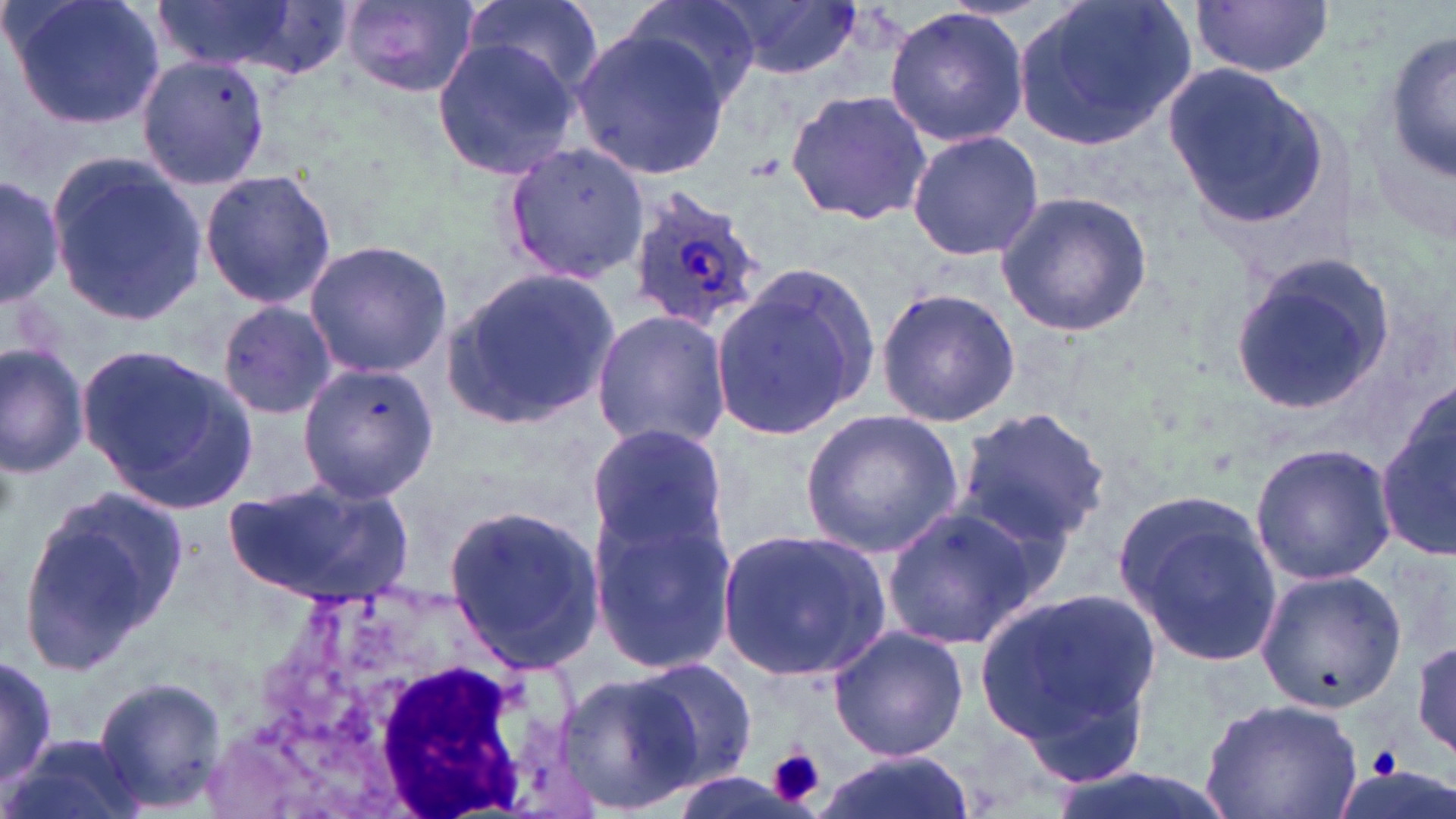
Summary:
  - Coordinate format: approximate bounding boxes as named x1/y1/x2/y2 corners in pixels
  - White blood cell locations: (x1=214, y1=587, x2=596, y2=819)
  - Plasmodium ovale-infected red blood cell locations: (x1=624, y1=186, x2=766, y2=335)
  - Uninfected red blood cell locations: (x1=6, y1=0, x2=165, y2=132), (x1=152, y1=0, x2=304, y2=74), (x1=336, y1=0, x2=482, y2=96), (x1=463, y1=0, x2=603, y2=97), (x1=624, y1=0, x2=761, y2=108), (x1=717, y1=0, x2=862, y2=81), (x1=1015, y1=0, x2=1194, y2=149), (x1=1191, y1=0, x2=1335, y2=78), (x1=883, y1=7, x2=1030, y2=145), (x1=571, y1=28, x2=733, y2=180), (x1=1385, y1=32, x2=1456, y2=187), (x1=429, y1=36, x2=585, y2=179), (x1=133, y1=53, x2=273, y2=192), (x1=1164, y1=64, x2=1331, y2=230), (x1=785, y1=86, x2=930, y2=226), (x1=905, y1=129, x2=1044, y2=262), (x1=500, y1=140, x2=649, y2=286), (x1=45, y1=152, x2=207, y2=326), (x1=199, y1=168, x2=337, y2=308), (x1=0, y1=170, x2=64, y2=312), (x1=994, y1=189, x2=1152, y2=338), (x1=303, y1=239, x2=452, y2=378), (x1=1223, y1=256, x2=1397, y2=416), (x1=709, y1=264, x2=879, y2=444), (x1=444, y1=267, x2=621, y2=429), (x1=875, y1=287, x2=1020, y2=428), (x1=216, y1=300, x2=338, y2=421), (x1=592, y1=310, x2=732, y2=450), (x1=0, y1=342, x2=88, y2=476), (x1=80, y1=344, x2=257, y2=510), (x1=298, y1=362, x2=439, y2=501), (x1=1380, y1=395, x2=1456, y2=562), (x1=952, y1=406, x2=1111, y2=552), (x1=800, y1=408, x2=963, y2=556), (x1=586, y1=423, x2=732, y2=565), (x1=1249, y1=442, x2=1397, y2=584), (x1=221, y1=476, x2=418, y2=604), (x1=1108, y1=485, x2=1283, y2=670), (x1=16, y1=486, x2=191, y2=676), (x1=587, y1=499, x2=736, y2=672), (x1=443, y1=503, x2=602, y2=675), (x1=880, y1=505, x2=1042, y2=650), (x1=718, y1=526, x2=891, y2=683), (x1=1253, y1=569, x2=1408, y2=711), (x1=975, y1=584, x2=1165, y2=781), (x1=830, y1=625, x2=972, y2=762), (x1=1412, y1=637, x2=1455, y2=760), (x1=1, y1=653, x2=56, y2=790), (x1=628, y1=657, x2=760, y2=790), (x1=556, y1=670, x2=700, y2=813), (x1=94, y1=677, x2=226, y2=808), (x1=1197, y1=697, x2=1364, y2=819), (x1=5, y1=734, x2=145, y2=819), (x1=812, y1=751, x2=978, y2=819)
  - Platelet locations: (x1=1368, y1=743, x2=1404, y2=780), (x1=770, y1=749, x2=825, y2=805)
  - Slide-level diagnosis: Plasmodium ovale
  - Modality: light microscopy
  - Image size: 1456×819 pixels
  - Preparation: thin blood smear
  - Field of view: one of a larger specimen
  - Stain: May-Grünwald-Giemsa
  - Magnification: 1000x